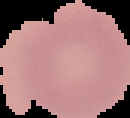

malaria_status: uninfected
image_size: 130×118 pixels
image_type: segmented cell region on a black background
preparation: thin blood film